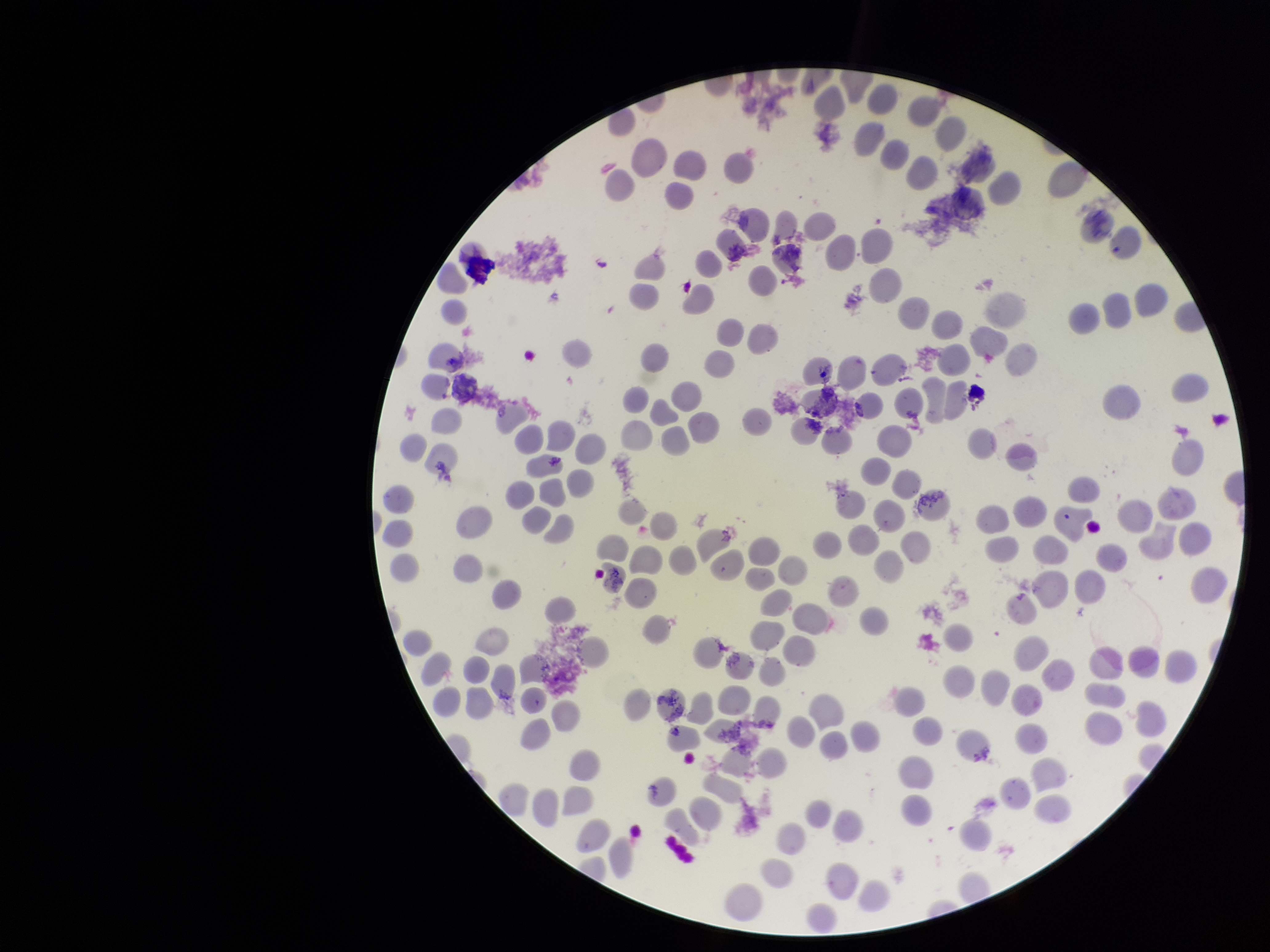
{
  "parasitized_red_blood_cells": "none seen",
  "parasitized_red_blood_cell_count": 0,
  "red_blood_cell_count": 217,
  "patient_malaria_status": "infected",
  "preparation": "thin smear",
  "field_of_view": "one from this slide",
  "image_size": "1270×952 pixels",
  "stain": "Giemsa",
  "species_reported_for_this_patient": "Plasmodium vivax",
  "capture": "smartphone photograph through the microscope eyepiece"
}